Name the blood parasite species.
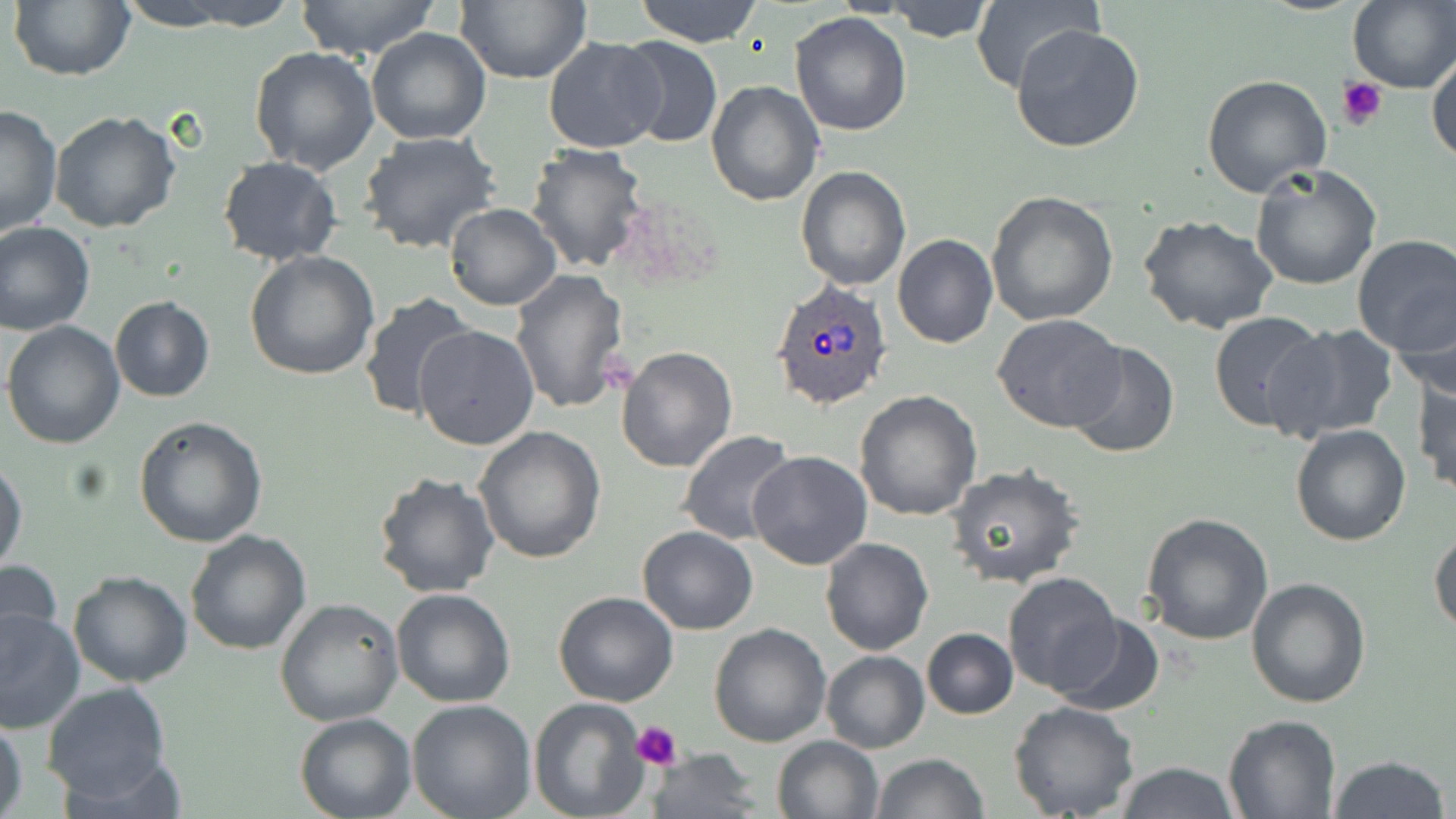

Plasmodium ovale.

field_of_view: single
platelet_locations: 'approximate bounding boxes as (x1, y1, x2, y2) in pixels: (1336, 75, 1388, 130), (630, 719, 683, 767)'
stain: May-Grünwald-Giemsa
image_size: 1456×819 pixels
preparation: thin blood film
uninfected_red_blood_cell_locations: 'approximate bounding boxes as (x1, y1, x2, y2) in pixels: (9, 0, 133, 82), (113, 0, 252, 31), (167, 0, 300, 30), (294, 0, 442, 59), (455, 0, 591, 85), (634, 0, 764, 47), (970, 0, 1099, 95), (1348, 0, 1456, 92), (883, 2, 996, 43), (790, 10, 912, 136), (1010, 22, 1146, 154), (366, 27, 492, 147), (615, 36, 723, 149), (542, 38, 667, 153), (250, 45, 381, 175), (1427, 52, 1455, 169), (1202, 72, 1333, 197), (706, 79, 824, 206), (0, 102, 63, 240), (49, 110, 182, 232), (357, 130, 502, 256), (524, 143, 651, 272), (217, 156, 343, 266), (1250, 163, 1383, 290), (795, 166, 910, 291), (984, 191, 1118, 327), (444, 203, 560, 310), (1138, 216, 1280, 335), (0, 220, 96, 335), (1351, 234, 1456, 356), (893, 235, 998, 348), (245, 250, 380, 381), (510, 269, 631, 416), (358, 291, 478, 422), (1390, 294, 1456, 405), (109, 295, 215, 403), (1208, 310, 1328, 432), (992, 313, 1125, 433), (2, 321, 126, 449), (1268, 323, 1401, 442), (413, 324, 539, 451), (1064, 340, 1179, 460), (617, 346, 738, 473), (1413, 371, 1455, 495), (855, 389, 983, 521), (133, 416, 268, 548), (1290, 423, 1412, 547), (473, 425, 606, 564), (678, 430, 798, 545), (747, 451, 872, 571), (0, 458, 26, 576), (944, 466, 1086, 591), (372, 470, 500, 598), (1141, 514, 1274, 645), (636, 526, 759, 635), (1429, 528, 1456, 637), (184, 529, 312, 655), (822, 536, 933, 655), (0, 557, 63, 658), (68, 570, 192, 688), (1003, 572, 1125, 696), (1244, 575, 1370, 709), (390, 588, 516, 708), (552, 591, 680, 707), (274, 596, 403, 726), (0, 607, 84, 734), (1049, 611, 1164, 716), (709, 624, 831, 748), (921, 628, 1018, 719), (821, 650, 929, 753), (42, 681, 172, 804), (407, 699, 536, 819), (529, 699, 649, 819), (1009, 701, 1141, 819), (295, 712, 416, 819), (0, 714, 27, 818), (1224, 714, 1341, 817), (771, 735, 883, 819), (648, 748, 764, 818), (871, 753, 988, 819), (1330, 756, 1449, 819), (1114, 761, 1240, 818)'
modality: light microscopy
plasmodium_ovale_infected_red_blood_cell_locations: 'approximate bounding boxes as (x1, y1, x2, y2) in pixels: (771, 280, 894, 411)'
magnification: 1000x